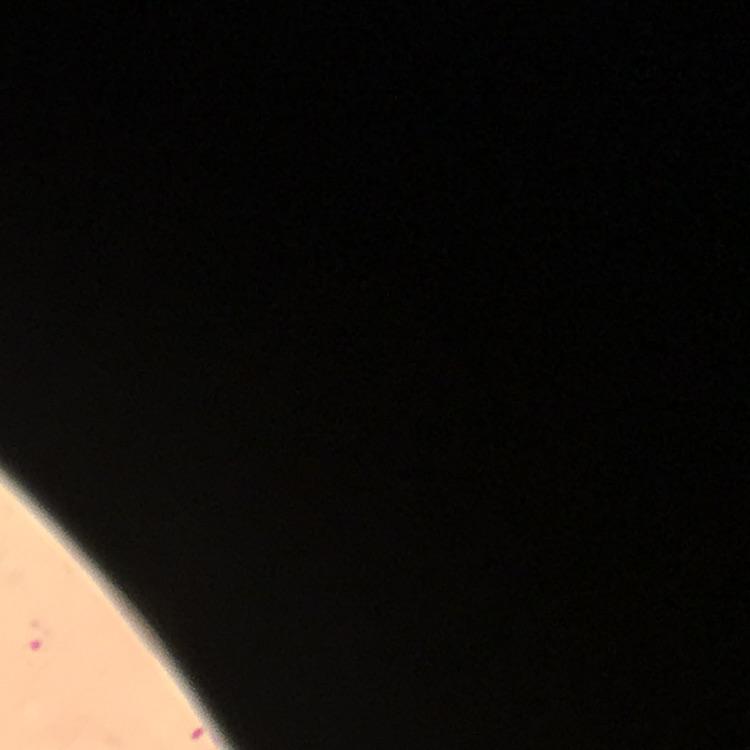
Approximate centers as (x, y) in pixels.
Summary:
  - Plasmodium parasite locations: (39, 637)
  - Capture: smartphone photograph through a microscope
  - Cropped from: one field of view
  - Immersion oil: applied
  - Context: from a malaria diagnostic workup
  - Image size: 750×750 pixels
  - Magnification: 100x
  - Preparation: thick smear
  - Stain: Giemsa